Find the red blood cells and label each as P. falciparum-infected, uninfected, or of indeterminate infection status.
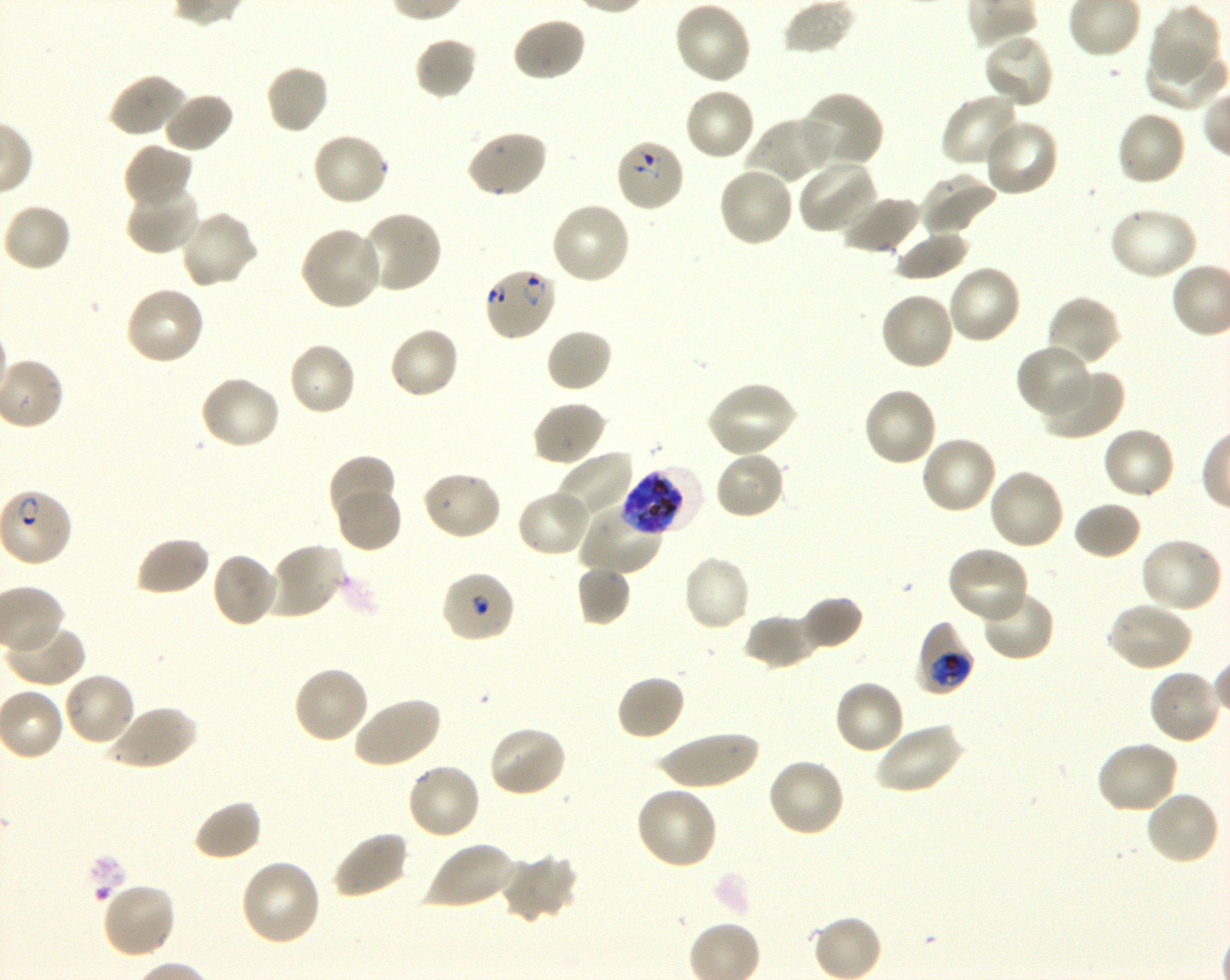

Approximate bounding boxes as {x1, y1, x2, y2} in pixels. Not every red blood cell is marked. A life-cycle stage — or a range of stages, where the recorded stages span more than one — follows each staged infected red blood cell.
Infected red blood cells: {615, 138, 687, 213} ring; {483, 266, 557, 342} ring; {620, 466, 703, 536} schizont; {915, 620, 974, 696} trophozoite.
Red blood cells of indeterminate infection status: {440, 570, 515, 644}.
Uninfected red blood cells: {674, 1, 753, 85}, {1149, 3, 1222, 84}, {511, 16, 587, 83}, {981, 32, 1054, 110}, {414, 36, 478, 100}, {1142, 42, 1227, 110}, {265, 63, 330, 136}, {108, 73, 186, 138}, {683, 86, 757, 161}, {800, 91, 886, 171}, {162, 92, 235, 154}, {940, 93, 1022, 172}, {1114, 110, 1188, 188}, {749, 116, 836, 184}, {982, 118, 1060, 198}, {464, 127, 548, 199}, {310, 131, 390, 207}, {122, 143, 194, 209}, {797, 159, 880, 235}, {716, 165, 795, 248}, {917, 173, 998, 237}, {126, 181, 201, 255}, {839, 193, 922, 256}, {549, 201, 633, 285}, {2, 203, 72, 274}, {1106, 206, 1198, 282}, {179, 210, 259, 290}, {360, 210, 443, 296}, {298, 224, 384, 312}, {893, 228, 971, 281}, {946, 265, 1023, 346}, {124, 286, 206, 367}, {878, 291, 955, 372}, {1045, 294, 1121, 368}, {388, 325, 460, 401}, {544, 328, 613, 393}, {286, 340, 357, 417}, {1015, 342, 1092, 418}, {1040, 367, 1124, 441}, {198, 374, 281, 452}, {706, 380, 797, 459}, {861, 385, 938, 468}, {531, 401, 608, 467}, {1101, 427, 1177, 502}, {918, 434, 998, 516}, {713, 449, 788, 520}, {555, 451, 636, 525}, {328, 455, 396, 524}, {987, 467, 1065, 552}, {421, 469, 503, 541}, {335, 487, 403, 553}, {515, 489, 592, 558}, {1073, 501, 1143, 561}, {579, 502, 664, 576}, {134, 535, 211, 598}, {1138, 537, 1224, 613}, {268, 542, 346, 620}, {946, 545, 1031, 623}, {210, 552, 279, 629}, {682, 554, 752, 632}, {576, 564, 632, 626}, {979, 587, 1055, 662}, {800, 596, 864, 651}, {1107, 601, 1193, 673}, {743, 612, 823, 669}, {4, 622, 84, 688}, {291, 664, 370, 745}, {1147, 667, 1222, 745}, {62, 671, 137, 748}, {616, 674, 687, 742}, {833, 679, 906, 756}, {350, 695, 442, 769}, {107, 704, 197, 772}, {873, 721, 965, 795}, {486, 724, 568, 798}, {654, 731, 760, 790}, {1095, 740, 1179, 815}, {766, 757, 847, 838}, {405, 761, 483, 841}, {635, 786, 719, 870}, {1143, 788, 1220, 866}, {192, 799, 263, 862}, {330, 831, 410, 900}, {422, 840, 516, 911}, {499, 853, 577, 924}, {239, 859, 322, 947}, {100, 881, 178, 960}.

objective = 100x, oil immersion, numerical aperture 1.30
life-cycle stages observed = ring, trophozoite, schizont
culture = shaking in-vitro P. falciparum strain 3D7
image size = 1230×980 pixels
stain = Giemsa
field of view = one from this slide
preparation = thin blood smear
donor blood group = O+